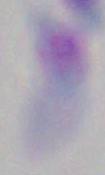 1000x magnification. Toxoplasma gondii is shown. Micrograph.